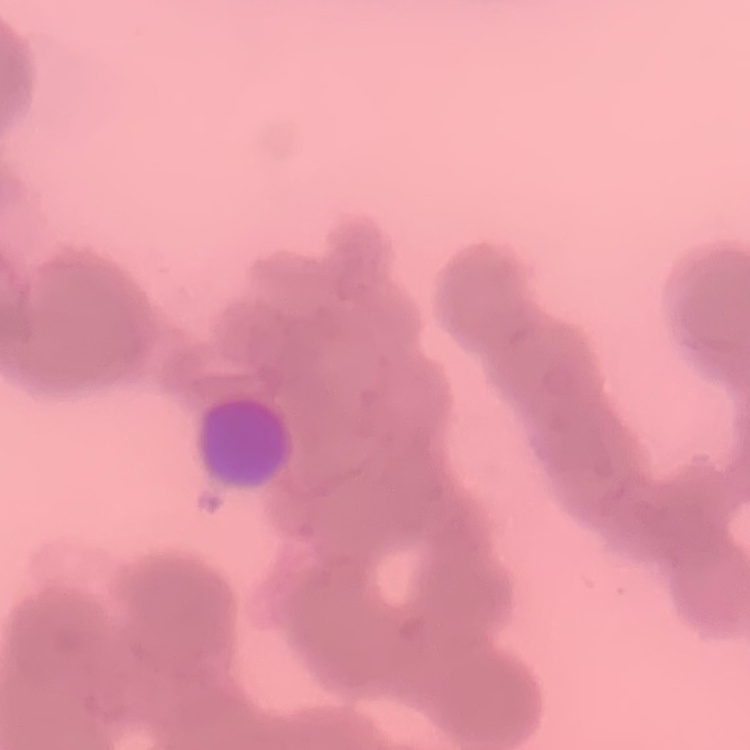

The erythrocytes exhibit rouleaux formation. Field's or Giemsa stain. Thin peripheral smear. Square crop of a larger photomicrograph.